Assess for parasitized red blood cells.
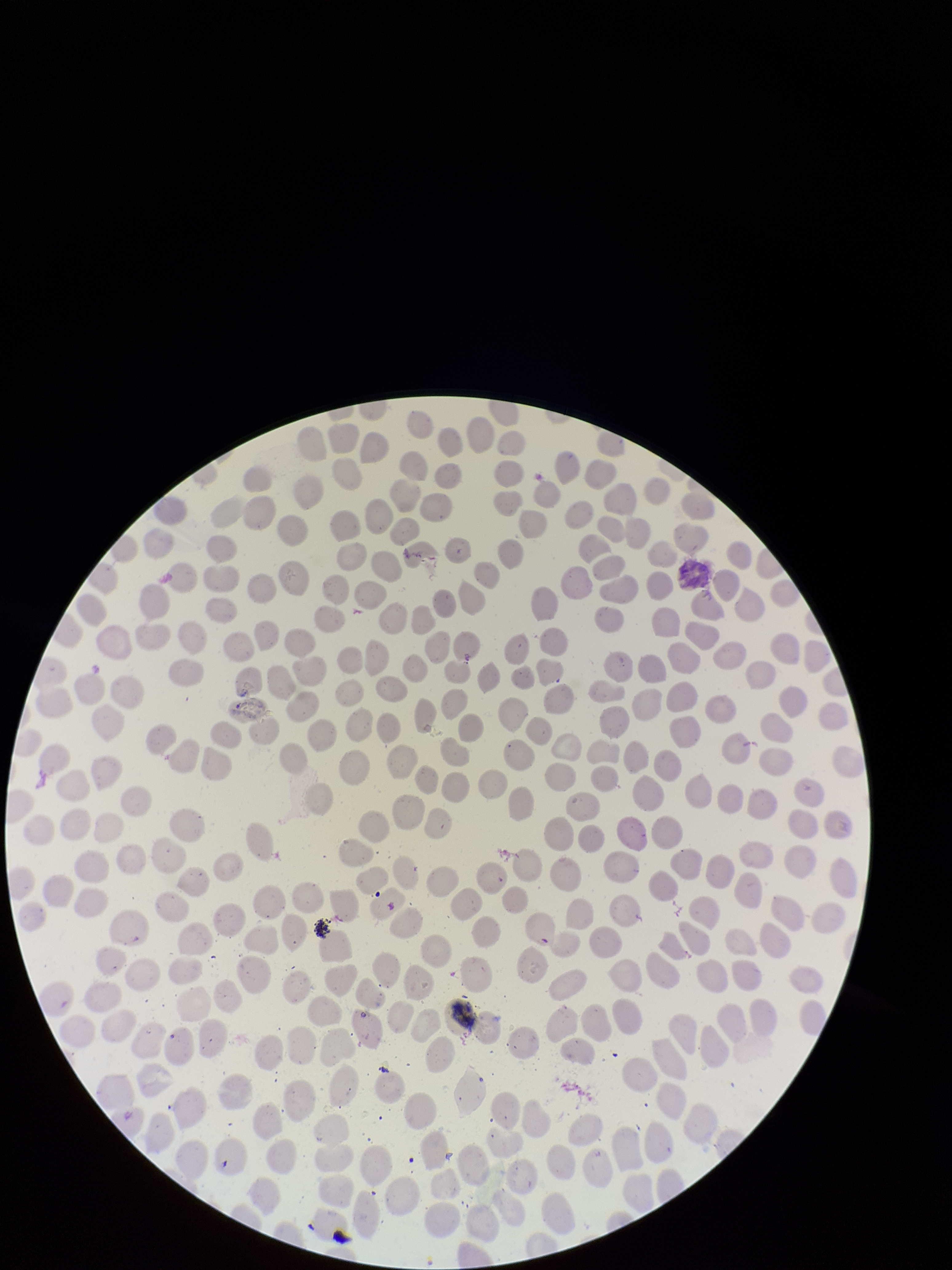
None seen.

Smartphone photograph taken through the eyepiece of a microscope. Single field of view. Image is 952×1270 pixels. Preparation: thin blood smear. Red blood cell count: 268. Giemsa stain. Patient malaria status: negative. Parasitized red blood cell count: 0.